Locate and identify every blood parasite.
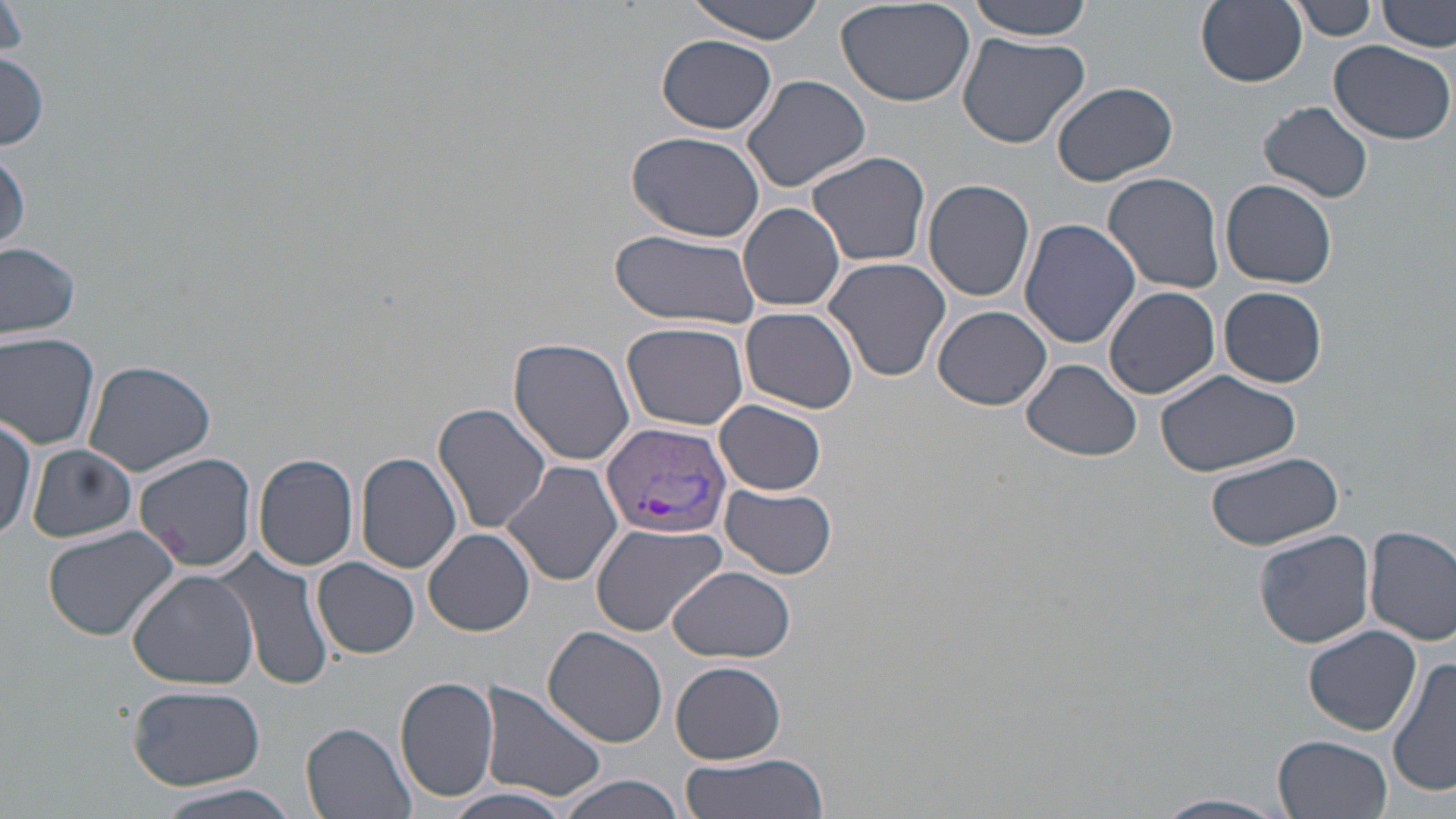

Approximate bounding boxes as [x1, y1, x2, y2] in pixels.
Plasmodium vivax-infected red blood cells: [601, 421, 733, 539].
No Plasmodium falciparum, Plasmodium ovale, Plasmodium malariae, Babesia divergens, or Trypanosoma brucei observed.

slide-level diagnosis = Plasmodium vivax
modality = optical microscopy
image size = 1456×819 pixels
preparation = thin blood film
uninfected red blood cell locations = approximate bounding boxes as [x1, y1, x2, y2] in pixels: [682, 0, 830, 42], [833, 0, 976, 107], [966, 0, 1095, 40], [1196, 0, 1307, 88], [1378, 0, 1455, 53], [1290, 1, 1376, 40], [0, 3, 29, 63], [956, 32, 1091, 149], [657, 35, 777, 133], [1327, 40, 1454, 143], [0, 52, 49, 150], [739, 74, 872, 192], [1053, 80, 1179, 187], [1257, 100, 1375, 204], [625, 130, 767, 241], [0, 150, 29, 253], [807, 150, 931, 267], [1102, 172, 1226, 295], [923, 178, 1035, 302], [1220, 178, 1338, 289], [739, 203, 845, 311], [1019, 218, 1141, 349], [610, 229, 763, 331], [0, 240, 83, 341], [822, 256, 952, 384], [1103, 285, 1221, 401], [1218, 286, 1327, 386], [933, 306, 1053, 412], [741, 307, 859, 415], [622, 320, 749, 429], [0, 333, 101, 449], [508, 336, 636, 465], [1020, 359, 1145, 462], [82, 360, 217, 477], [1154, 368, 1300, 476], [714, 400, 828, 494], [434, 401, 553, 537], [0, 411, 43, 540], [26, 445, 137, 542], [354, 450, 461, 574], [133, 451, 258, 573], [1203, 452, 1345, 550], [253, 454, 359, 570], [502, 461, 624, 587], [720, 483, 837, 579], [589, 522, 726, 636], [43, 523, 182, 642], [1365, 525, 1456, 645], [425, 528, 534, 636], [1253, 530, 1374, 648], [219, 547, 335, 693], [312, 558, 420, 658], [669, 566, 796, 663], [127, 569, 259, 689], [1303, 625, 1422, 734], [544, 627, 669, 749], [1388, 656, 1455, 798], [671, 660, 786, 764], [394, 676, 501, 805], [479, 680, 607, 805], [128, 685, 267, 789], [301, 723, 417, 819], [1274, 733, 1393, 819], [676, 752, 830, 818], [555, 775, 686, 818], [148, 781, 304, 819], [442, 786, 577, 819], [1154, 794, 1289, 818]
magnification = 1000x
field of view = one of a larger specimen
stain = May-Grünwald-Giemsa